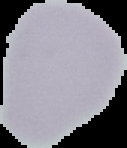
Summary:
  - Preparation: thin blood film
  - Image size: 127×148 pixels
  - Image type: segmented cell region on a black background
  - Result: no Plasmodium parasites seen